Assess the morphology of the red blood cells.
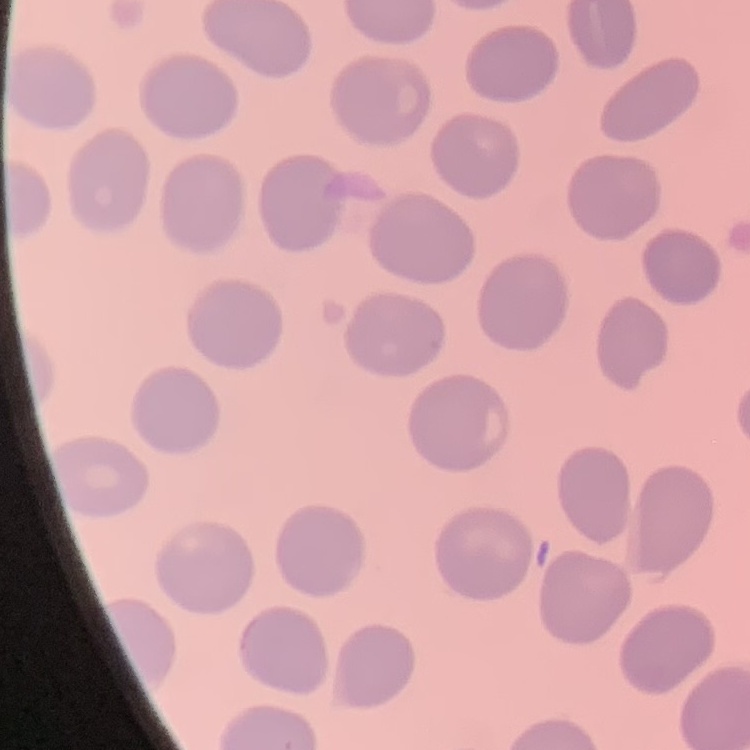

They show no rouleaux formation.

preparation = thin blood smear
image type = square crop of a larger photomicrograph
stain = Field's or Giemsa